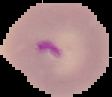
preparation = thin blood smear
malaria status = parasitized
image type = segmented cell region on a black background
image size = 112×97 pixels